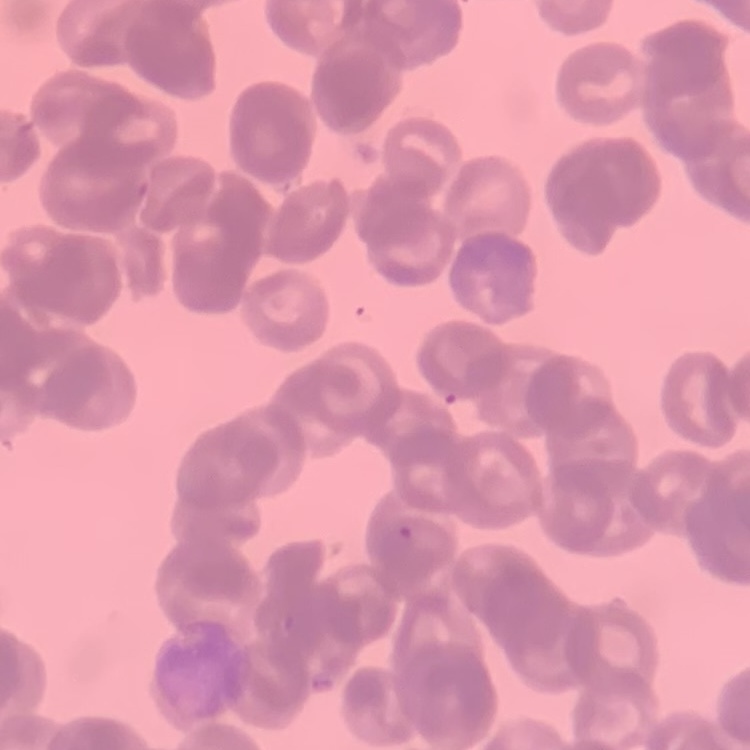

Summary:
  - Red blood cell morphology: rouleaux formation
  - Stain: Field's or Giemsa
  - Preparation: thin blood film
  - Image type: one tile cut from a larger photomicrograph